Assess the morphology of the red blood cells.
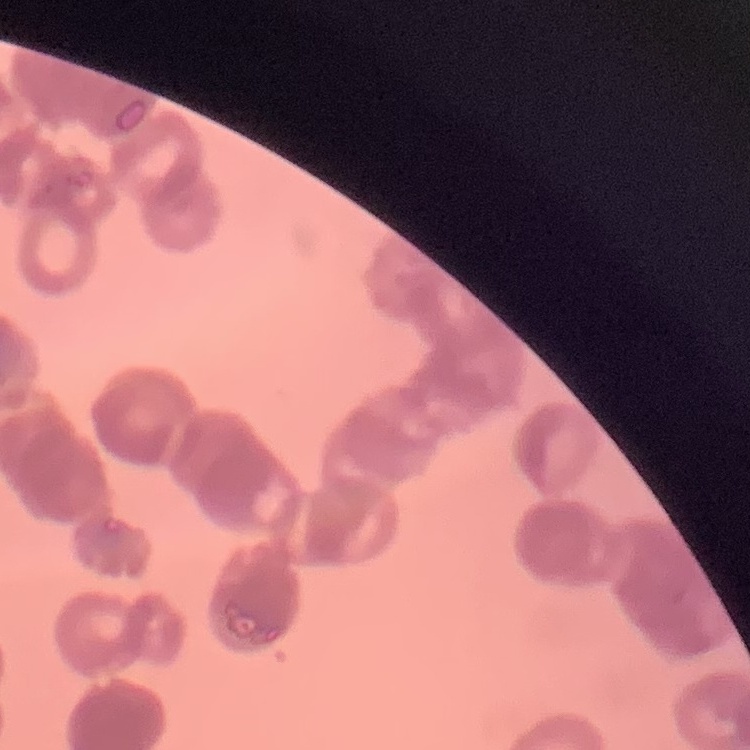

They show rouleaux formation.

Summary:
  - Preparation: thin blood film
  - Stain: Field's or Giemsa
  - Image type: one tile cut from a larger photomicrograph